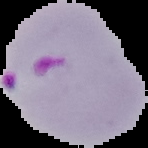

Summary:
  - Image type: segmented cell region on a black background
  - Preparation: thin blood smear
  - Image size: 148×148 pixels
  - Malaria status: parasitized